Locate every blood parasite and identify its species.
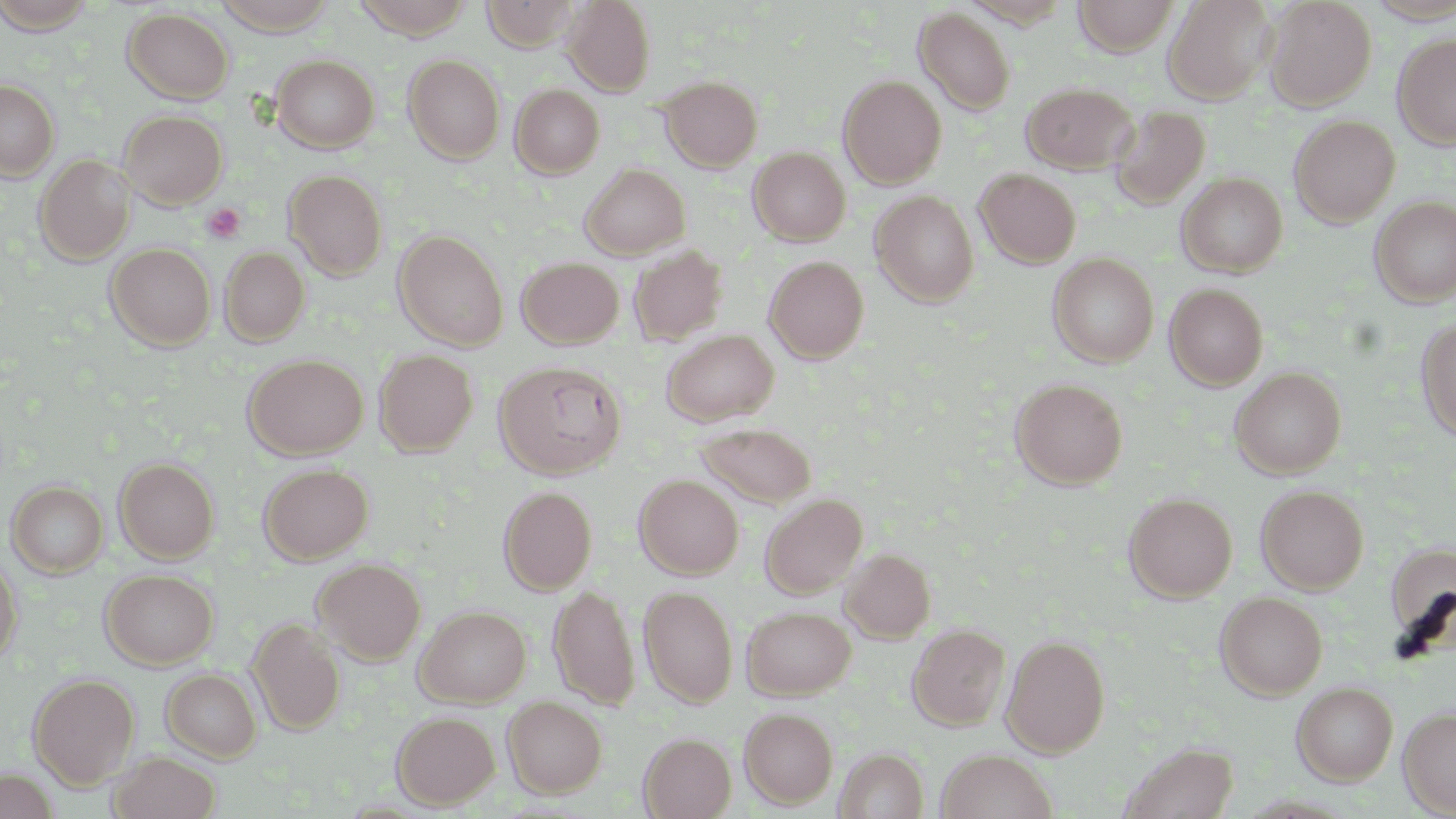

No blood parasites observed.

slide-level diagnosis = no evidence of blood parasites
uninfected red blood cell locations = approximate bounding boxes as [x1, y1, x2, y2] in pixels: [0, 0, 99, 33], [210, 0, 340, 33], [351, 0, 476, 38], [482, 0, 580, 50], [562, 0, 655, 95], [1073, 0, 1179, 56], [1164, 0, 1276, 103], [1264, 0, 1376, 110], [914, 7, 1017, 115], [122, 8, 234, 103], [1393, 33, 1456, 150], [271, 54, 379, 153], [404, 55, 505, 164], [659, 75, 762, 172], [839, 75, 947, 188], [0, 79, 59, 179], [1022, 81, 1137, 174], [511, 84, 604, 179], [1108, 104, 1211, 209], [118, 109, 228, 208], [1289, 115, 1400, 227], [748, 146, 851, 246], [34, 154, 135, 265], [581, 163, 691, 259], [975, 168, 1081, 268], [284, 169, 388, 280], [1177, 173, 1288, 277], [871, 191, 979, 306], [1371, 196, 1456, 306], [393, 230, 509, 350], [106, 243, 216, 349], [629, 245, 728, 345], [220, 246, 310, 346], [1048, 252, 1159, 367], [764, 255, 869, 362], [517, 256, 625, 349], [1165, 283, 1269, 390], [1416, 319, 1456, 444], [661, 329, 780, 426], [374, 348, 478, 456], [244, 354, 368, 459], [495, 360, 627, 479], [1229, 367, 1346, 479], [1010, 378, 1129, 490], [696, 422, 817, 508], [115, 457, 219, 562], [259, 462, 373, 565], [634, 474, 743, 579], [8, 480, 108, 577], [1256, 484, 1368, 594], [498, 486, 596, 595], [1124, 492, 1237, 601], [760, 494, 867, 598], [1385, 542, 1456, 650], [841, 548, 935, 643], [0, 554, 23, 664], [312, 558, 426, 665], [101, 569, 218, 669], [549, 584, 639, 709], [639, 585, 738, 708], [1215, 592, 1327, 699], [414, 605, 532, 706], [742, 605, 856, 699], [247, 617, 346, 736], [908, 623, 1010, 730], [1002, 635, 1110, 756], [162, 668, 261, 762], [29, 673, 139, 787], [1292, 682, 1399, 784], [502, 696, 607, 798], [738, 707, 838, 809], [1398, 707, 1456, 817], [391, 710, 499, 810], [639, 732, 736, 818], [1119, 741, 1238, 819], [835, 748, 929, 819], [935, 749, 1058, 819], [109, 752, 221, 819]
preparation = thin blood smear
stain = May-Grünwald-Giemsa
field of view = one of a larger specimen
image size = 1456×819 pixels
platelet locations = approximate bounding boxes as [x1, y1, x2, y2] in pixels: [202, 203, 245, 244]
modality = optical microscopy
magnification = 1000x